Report the malaria status of this cell.
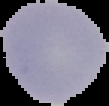
Uninfected.

Image is 109×106 pixels. Segmented cell region on a black background. From a thin blood smear.